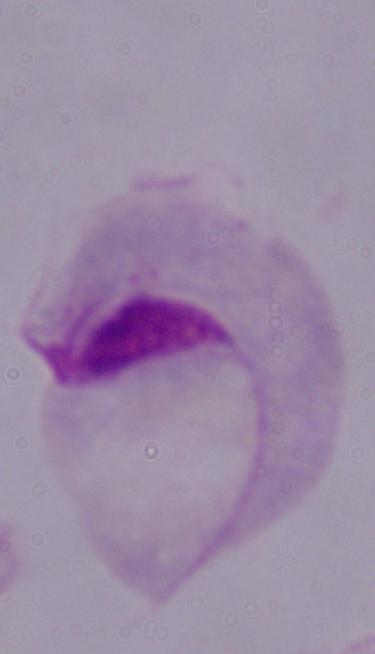

{
  "magnification": "1000x",
  "modality": "photomicrograph",
  "identification": "trichomonad"
}